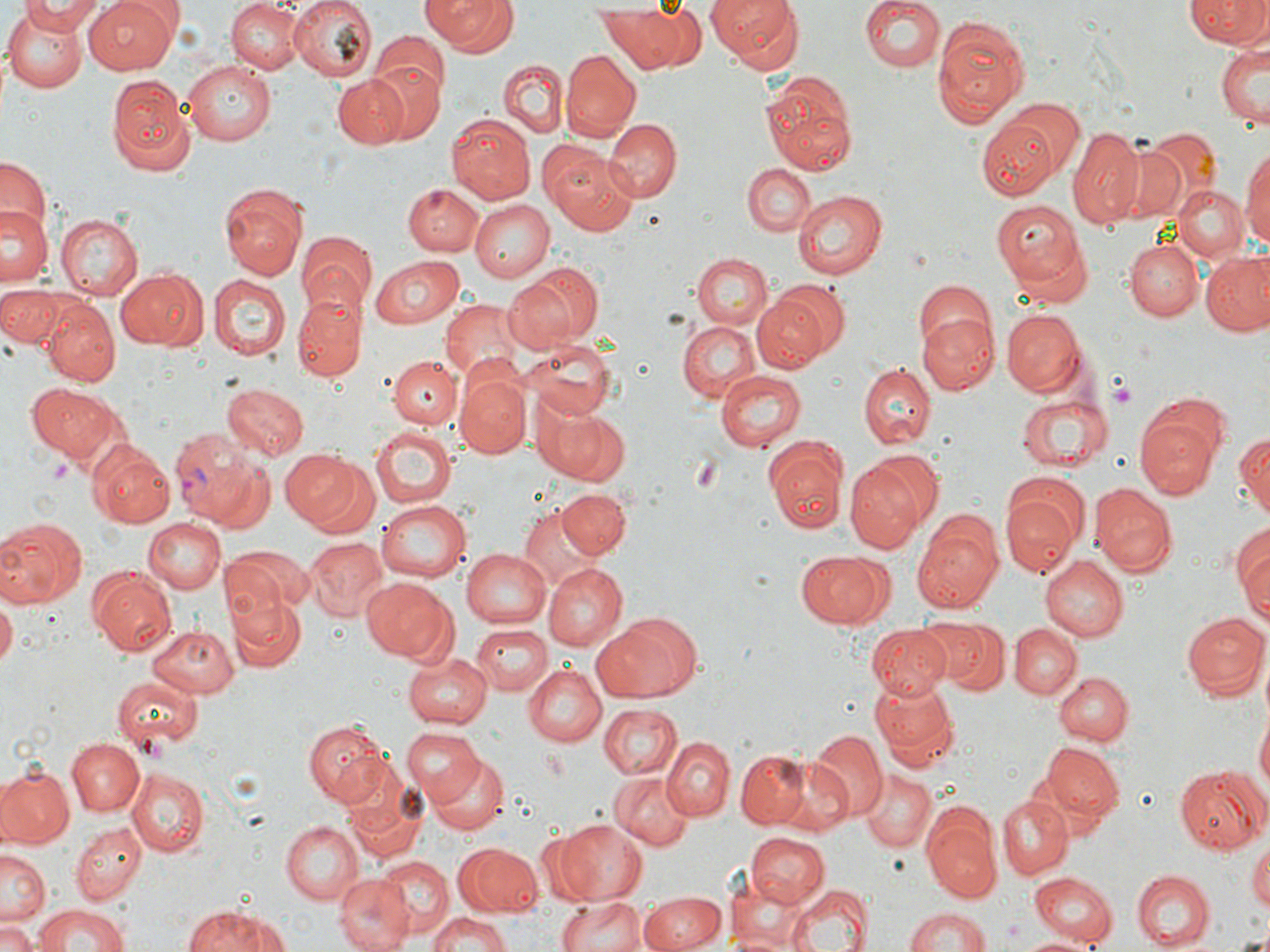

slide-level diagnosis = Plasmodium vivax
preparation = thin blood film
image size = 1270×952 pixels
platelet locations = approximate bounding boxes as (x1, y1, x2, y2) in pixels: (1105, 374, 1141, 410), (686, 453, 726, 497)
modality = optical microscopy
uninfected red blood cell locations = approximate bounding boxes as (x1, y1, x2, y2) in pixels: (16, 0, 103, 34), (84, 0, 179, 74), (227, 0, 303, 74), (287, 0, 376, 83), (422, 0, 517, 57), (704, 0, 805, 75), (860, 0, 944, 73), (1185, 0, 1266, 49), (596, 3, 688, 73), (1, 5, 92, 93), (372, 15, 454, 110), (932, 16, 1030, 126), (1215, 39, 1269, 131), (562, 51, 640, 141), (364, 57, 446, 146), (181, 59, 276, 144), (498, 59, 567, 140), (761, 70, 856, 174), (333, 73, 411, 148), (105, 75, 195, 176), (1005, 99, 1085, 178), (980, 112, 1072, 198), (446, 114, 535, 204), (604, 117, 680, 200), (1068, 128, 1148, 228), (1146, 128, 1221, 204), (1107, 142, 1189, 224), (1241, 145, 1270, 257), (549, 154, 640, 234), (0, 155, 51, 242), (743, 163, 815, 235), (218, 182, 307, 282), (402, 182, 486, 256), (1173, 186, 1248, 265), (793, 189, 889, 279), (993, 199, 1086, 286), (471, 200, 553, 282), (1, 207, 49, 289), (57, 214, 144, 298), (300, 228, 378, 316), (1126, 238, 1201, 321), (1202, 250, 1270, 337), (694, 253, 772, 329), (371, 255, 464, 329), (511, 260, 606, 348), (114, 268, 206, 350), (208, 274, 289, 358), (913, 279, 995, 360), (772, 280, 849, 361), (1, 282, 71, 351), (752, 294, 829, 373), (294, 296, 364, 383), (439, 300, 527, 385), (43, 301, 121, 387), (1000, 306, 1084, 395), (918, 313, 999, 394), (677, 319, 761, 402), (520, 337, 618, 420), (389, 357, 459, 430), (858, 364, 935, 451), (715, 370, 807, 454), (456, 373, 531, 458), (220, 381, 307, 461), (27, 382, 121, 466), (1018, 392, 1111, 474), (533, 398, 622, 483), (1136, 413, 1222, 499), (370, 426, 455, 508), (1235, 428, 1269, 519), (764, 434, 847, 533), (90, 443, 176, 528), (278, 450, 362, 529), (867, 450, 943, 526), (202, 458, 276, 536), (846, 462, 926, 551), (998, 474, 1086, 575), (1091, 486, 1176, 577), (557, 489, 630, 560), (374, 498, 471, 583), (519, 504, 606, 590), (913, 509, 1004, 613), (0, 516, 88, 610), (142, 518, 224, 593), (1233, 523, 1270, 623), (303, 537, 387, 621), (224, 543, 312, 622), (460, 549, 550, 626), (794, 550, 895, 628), (1041, 555, 1128, 640), (543, 565, 626, 649), (90, 569, 175, 658), (361, 576, 452, 659), (230, 594, 305, 673), (0, 596, 17, 667), (1183, 611, 1268, 700), (591, 614, 694, 704), (937, 619, 1008, 694), (471, 623, 553, 695), (1009, 623, 1081, 699), (146, 624, 241, 697), (868, 627, 953, 700), (401, 651, 491, 727), (521, 664, 606, 746), (1053, 671, 1131, 746), (112, 676, 201, 751), (871, 679, 957, 766), (597, 704, 683, 780), (1254, 710, 1269, 804), (301, 719, 392, 808), (400, 728, 484, 805), (808, 730, 887, 820), (66, 737, 143, 817), (665, 739, 734, 819), (1041, 744, 1125, 824), (0, 750, 125, 838), (734, 751, 811, 828), (759, 752, 854, 834), (426, 754, 508, 836), (1174, 765, 1267, 854), (0, 766, 74, 847), (127, 768, 208, 856), (859, 772, 935, 852), (609, 774, 696, 851), (998, 793, 1074, 878), (921, 810, 1002, 903), (551, 817, 647, 905), (73, 821, 147, 905), (280, 821, 363, 905), (745, 832, 829, 907), (1249, 839, 1270, 912), (453, 843, 547, 915), (1, 851, 47, 927), (376, 855, 452, 933), (1131, 870, 1214, 949), (333, 872, 415, 952), (1029, 874, 1117, 945), (789, 884, 871, 952), (639, 891, 726, 951), (554, 897, 654, 952), (179, 902, 292, 952), (32, 904, 131, 952), (904, 906, 988, 952), (423, 911, 512, 952), (0, 920, 40, 952), (1234, 932, 1270, 951), (1023, 935, 1097, 952)
field of view = single
stain = May-Grünwald-Giemsa
Plasmodium vivax-infected red blood cell locations = approximate bounding boxes as (x1, y1, x2, y2) in pixels: (168, 426, 261, 520)
magnification = 1000x